Identify the parasite.
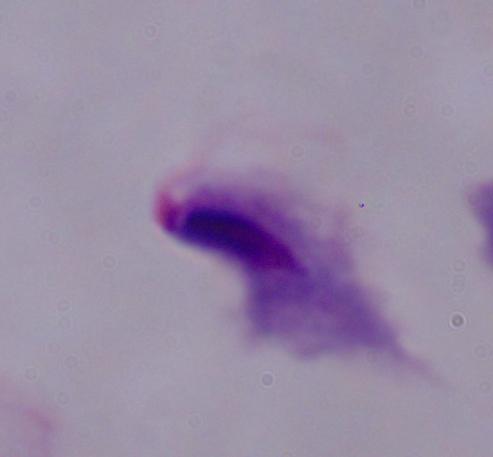
A trichomonad.

magnification = 1000x
modality = photomicrograph